Describe the morphology of the erythrocytes.
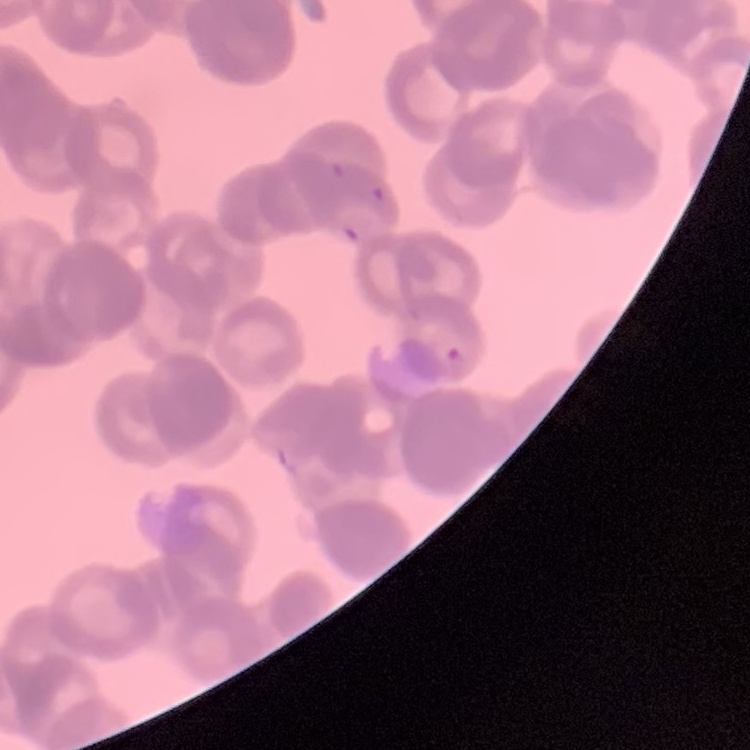
Rouleaux formation.

Summary:
  - Image type: square crop of a larger photomicrograph
  - Stain: Field's or Giemsa
  - Preparation: thin blood film